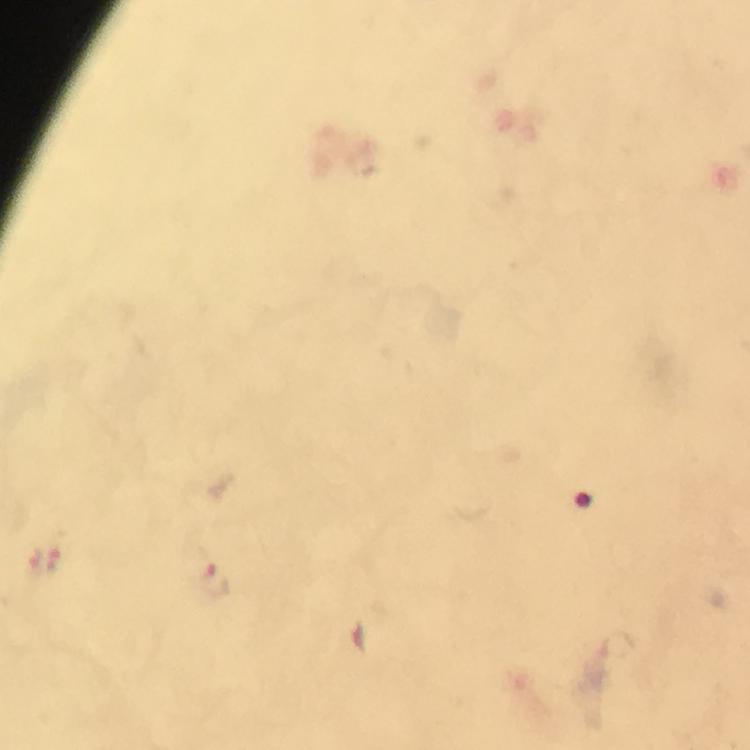
cropped from = one field of view
stain = Giemsa
image size = 750×750 pixels
preparation = thick smear
magnification = 100x
Plasmodium parasite locations = approximate centers as [x, y] in pixels: [215, 582]
immersion oil = used
capture = smartphone camera through the microscope
context = from a malaria diagnostic workup